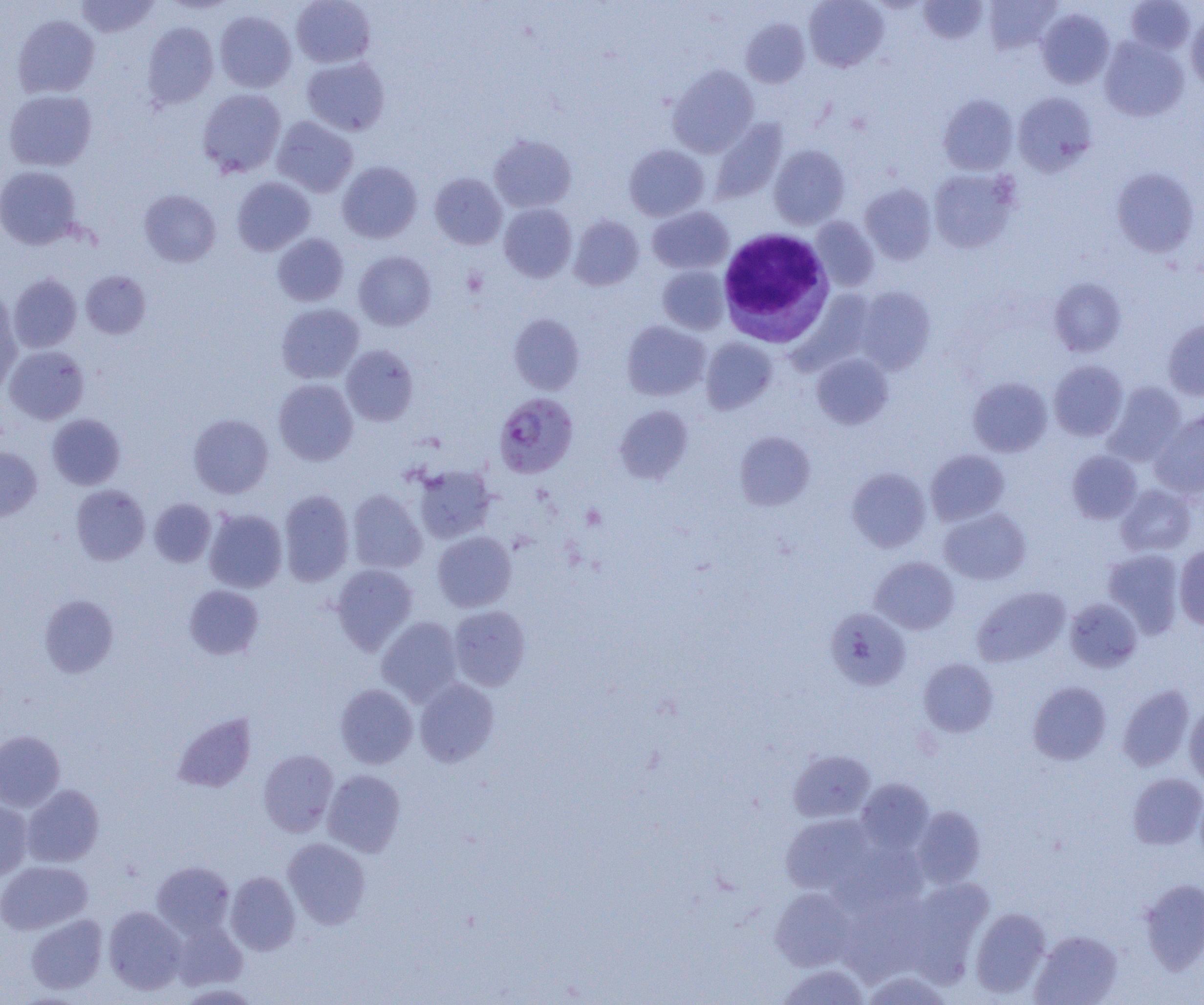

Approximate bounding boxes as [x1, y1, x2, y2] in pixels. Plasmodium falciparum-infected red blood cell locations: [494, 392, 578, 478]. Platelet locations: [462, 268, 488, 297]. White blood cell locations: [717, 228, 835, 347]. Uninfected red blood cell locations: [75, 0, 160, 38], [291, 0, 376, 68], [804, 0, 888, 72], [918, 0, 988, 44], [984, 0, 1062, 53], [1125, 0, 1196, 55], [1037, 8, 1115, 88], [214, 11, 296, 93], [1186, 11, 1204, 93], [13, 14, 100, 98], [741, 18, 810, 87], [142, 22, 218, 108], [1099, 37, 1188, 122], [302, 57, 390, 135], [668, 64, 759, 157], [197, 88, 286, 177], [3, 89, 97, 171], [1013, 92, 1097, 175], [939, 94, 1018, 175], [272, 116, 358, 197], [710, 118, 788, 204], [489, 134, 577, 212], [624, 144, 709, 221], [769, 145, 850, 229], [337, 161, 422, 243], [0, 165, 82, 249], [1111, 167, 1200, 257], [928, 168, 1019, 253], [430, 173, 507, 250], [232, 177, 315, 255], [860, 183, 936, 264], [139, 189, 220, 267], [499, 203, 577, 282], [647, 206, 734, 274], [568, 215, 644, 290], [811, 216, 879, 291], [272, 233, 349, 306], [354, 251, 436, 331], [657, 265, 730, 334], [81, 270, 151, 339], [8, 273, 81, 353], [1049, 278, 1126, 357], [855, 286, 936, 374], [0, 292, 20, 393], [276, 303, 364, 384], [508, 314, 585, 394], [1163, 319, 1204, 400], [622, 320, 710, 401], [700, 338, 777, 414], [4, 345, 89, 424], [341, 345, 419, 426], [812, 353, 893, 429], [1049, 360, 1128, 440], [968, 377, 1052, 457], [274, 379, 358, 465], [1103, 382, 1186, 466], [615, 405, 693, 483], [1150, 410, 1204, 497], [47, 413, 125, 490], [188, 413, 273, 498], [735, 431, 815, 510], [0, 447, 42, 521], [926, 449, 1009, 525], [1067, 450, 1142, 523], [412, 464, 496, 543], [846, 467, 931, 552], [71, 484, 150, 565], [1116, 484, 1197, 556], [278, 489, 354, 586], [347, 489, 427, 574], [149, 498, 216, 567], [940, 507, 1031, 585], [204, 508, 287, 593], [432, 531, 516, 612], [1174, 545, 1204, 629], [1103, 549, 1185, 639], [869, 556, 959, 634], [331, 563, 418, 655], [183, 585, 264, 659], [972, 586, 1070, 666], [39, 594, 119, 677], [1065, 598, 1142, 672], [449, 605, 531, 690], [826, 608, 912, 690], [377, 616, 463, 705], [919, 658, 998, 737], [414, 677, 500, 767], [1028, 681, 1111, 764], [335, 684, 417, 768], [1117, 684, 1195, 772], [1184, 703, 1204, 788], [172, 712, 256, 792], [0, 730, 65, 812], [258, 749, 339, 837], [788, 749, 876, 823], [323, 769, 406, 857], [1128, 773, 1204, 850], [856, 778, 934, 854], [21, 784, 104, 867], [0, 800, 33, 881], [911, 806, 986, 888], [780, 813, 879, 896], [283, 838, 371, 929], [830, 842, 928, 918], [0, 861, 93, 934], [151, 861, 235, 939], [225, 871, 300, 955], [907, 877, 994, 980], [1139, 879, 1204, 974], [770, 887, 857, 971], [839, 900, 928, 984], [104, 906, 186, 994], [970, 907, 1051, 998], [25, 914, 108, 994], [171, 919, 248, 991], [1031, 930, 1122, 1005], [776, 963, 870, 1005], [859, 969, 955, 1004]. Slide-level diagnosis: Plasmodium falciparum. One field of a larger specimen. Thin blood film. Image is 1204×1005 pixels. Captured at 1000x magnification. Optical microscopy.